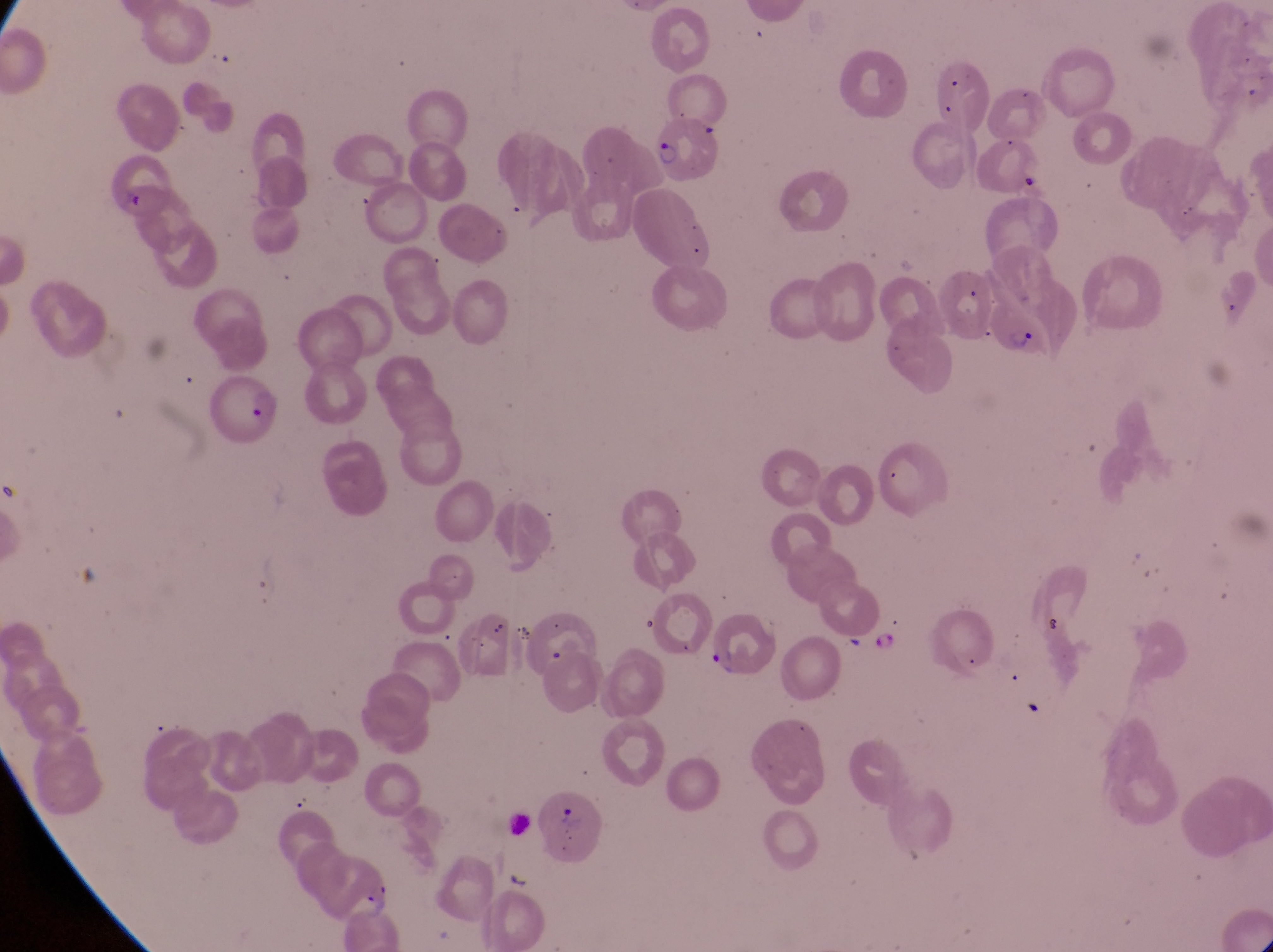

capture = smartphone photograph through the eyepiece of an Olympus CX-23 microscope
field of view = single
trophozoite locations = approximate bounding boxes as [left, top, right, bottom] in pixels: [1208, 265, 1245, 322], [869, 626, 902, 659]
artifact (platelet-like body, stain precipitate, or debris) locations = approximate bounding boxes as [left, top, right, bottom] in pixels: [505, 867, 535, 902]
parasitised red blood cell locations = approximate bounding boxes as [left, top, right, bottom] in pixels: [647, 104, 725, 187], [989, 280, 1088, 363], [205, 375, 282, 442], [712, 607, 784, 681], [534, 791, 606, 863]
image size = 1273×952 pixels
country = Uganda
magnification = 1000x
preparation = thin blood film